State which cell type is depicted.
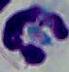
A leukocyte.

{
  "magnification": "1000x",
  "modality": "micrograph"
}